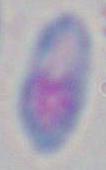 Micrograph. 1000x magnification. Toxoplasma gondii is shown.